Name the parasite shown.
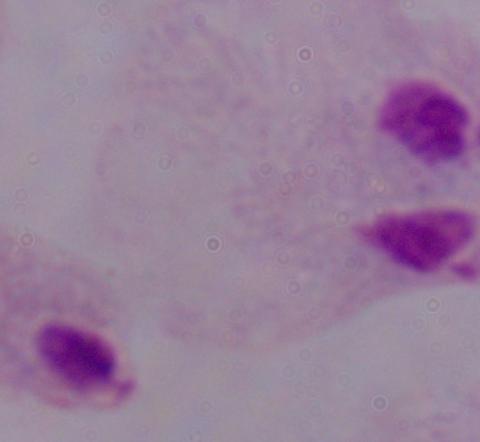
A trichomonad.

Photomicrograph. 1000x magnification.